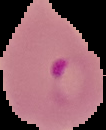

Summary:
  - Image size: 106×130 pixels
  - Preparation: thin blood film
  - Result: Plasmodium parasites identified
  - Image type: cell region segmented out of the field of view; surrounding area masked to black